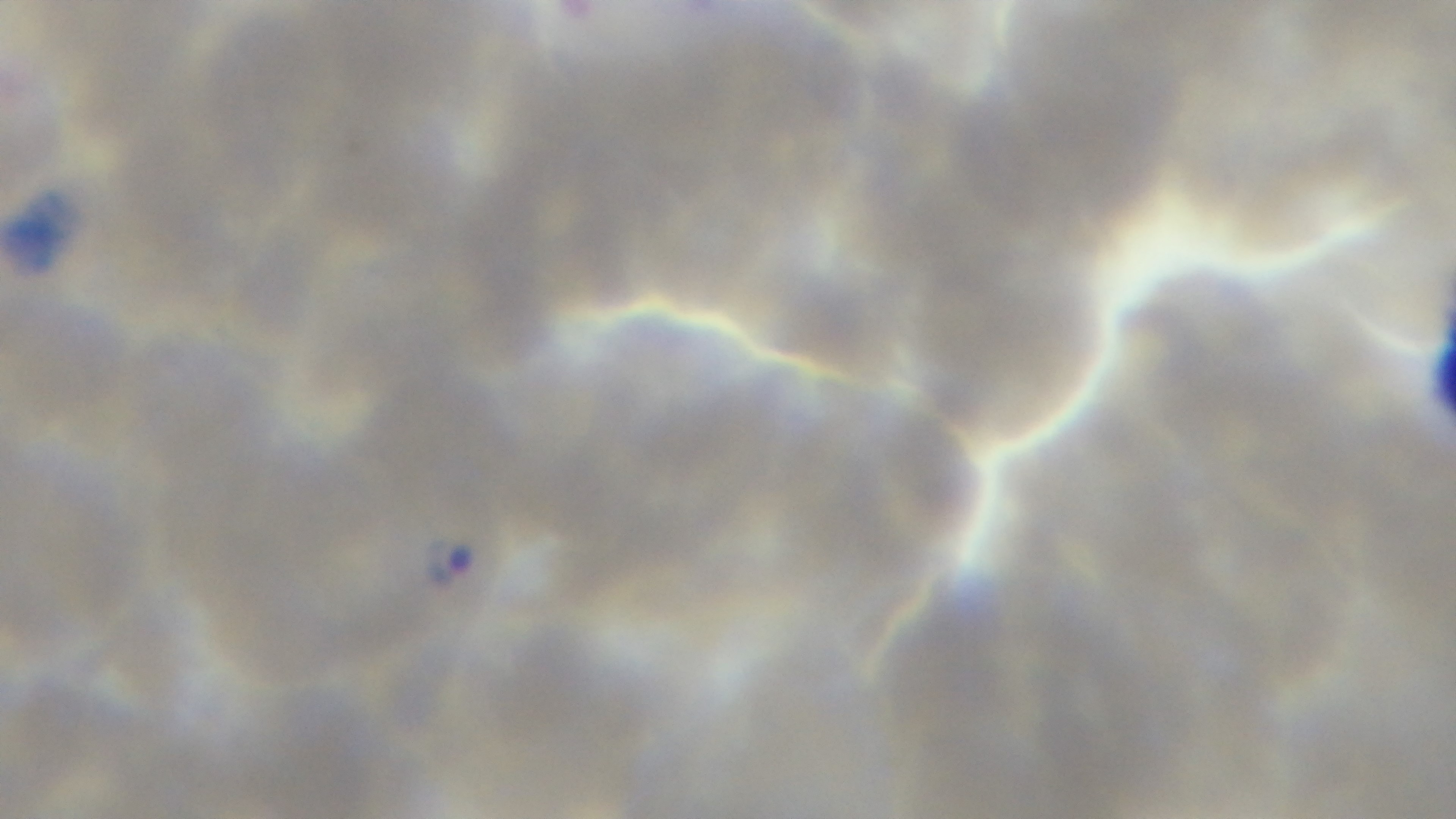

stain = Giemsa
modality = light microscopy
objective = 100x oil immersion
capture = mounted 4K digital camera
preparation = thin
field of view = one from the slide
malaria status = positive